Assess this cell for malaria.
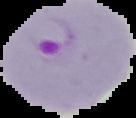
Parasitized.

Summary:
  - Image type: segmented cell region with the area outside set to black
  - Image size: 136×118 pixels
  - Preparation: thin blood smear